State which parasite is depicted.
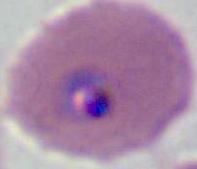
Plasmodium.

Summary:
  - Modality: photomicrograph
  - Magnification: 400x or 1000x